Assess the morphology of the erythrocytes.
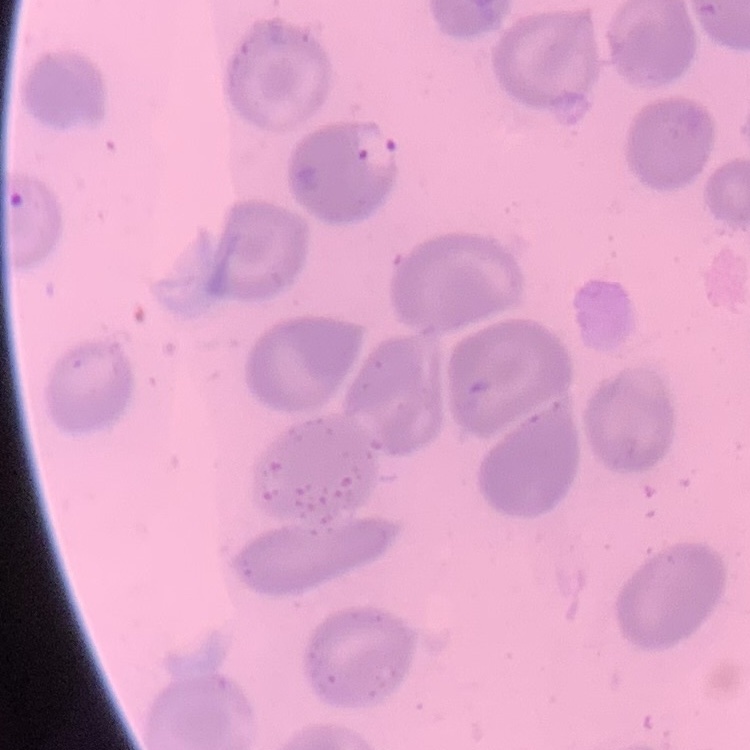
They show no rouleaux formation.

One tile cut from a larger photomicrograph. Thin blood film. Stained with either Field's or Giemsa.